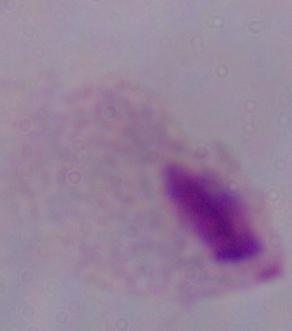

Summary:
  - Magnification: 1000x
  - Modality: photomicrograph
  - Identification: trichomonad